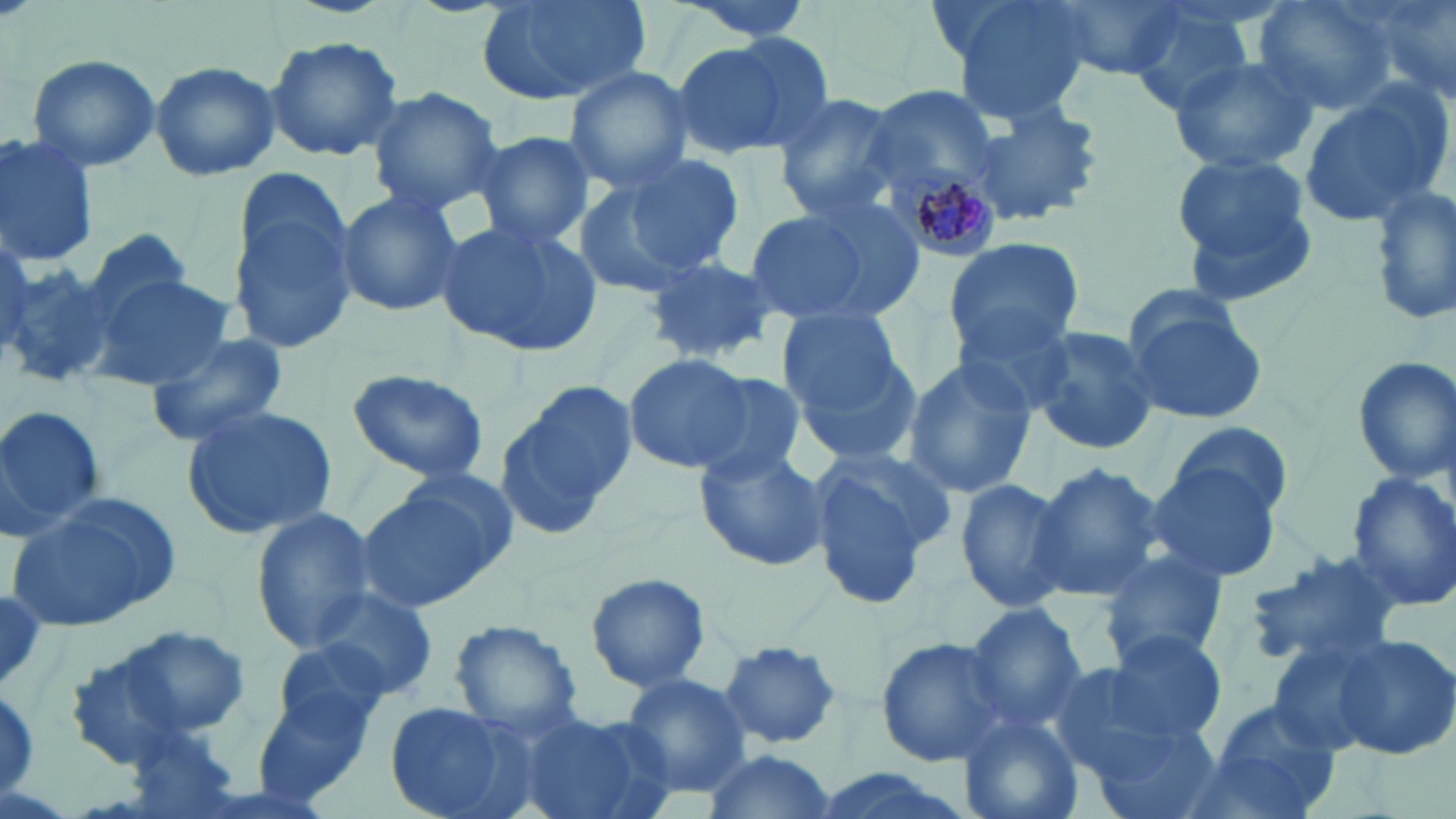

slide_level_diagnosis: Plasmodium malariae
modality: optical microscopy
uninfected_red_blood_cell_locations: 'approximate bounding boxes as named x1/y1/x2/y2 corners in pixels: (x1=475, y1=0, x2=648, y2=106), (x1=668, y1=0, x2=823, y2=42), (x1=941, y1=0, x2=1095, y2=125), (x1=1049, y1=0, x2=1187, y2=80), (x1=1125, y1=0, x2=1260, y2=111), (x1=1253, y1=0, x2=1397, y2=116), (x1=1358, y1=0, x2=1455, y2=110), (x1=672, y1=34, x2=827, y2=162), (x1=265, y1=35, x2=404, y2=162), (x1=26, y1=53, x2=161, y2=174), (x1=1167, y1=53, x2=1319, y2=174), (x1=150, y1=58, x2=281, y2=181), (x1=562, y1=65, x2=696, y2=190), (x1=363, y1=83, x2=506, y2=217), (x1=856, y1=83, x2=999, y2=189), (x1=1299, y1=83, x2=1452, y2=227), (x1=768, y1=90, x2=904, y2=221), (x1=963, y1=96, x2=1106, y2=228), (x1=472, y1=130, x2=597, y2=248), (x1=0, y1=133, x2=100, y2=268), (x1=613, y1=152, x2=745, y2=278), (x1=1170, y1=152, x2=1320, y2=299), (x1=226, y1=168, x2=361, y2=349), (x1=568, y1=175, x2=694, y2=298), (x1=1369, y1=186, x2=1456, y2=327), (x1=334, y1=188, x2=463, y2=318), (x1=739, y1=200, x2=909, y2=328), (x1=437, y1=219, x2=604, y2=358), (x1=73, y1=227, x2=197, y2=342), (x1=943, y1=237, x2=1085, y2=359), (x1=644, y1=256, x2=784, y2=366), (x1=0, y1=260, x2=120, y2=392), (x1=86, y1=269, x2=231, y2=394), (x1=1121, y1=300, x2=1264, y2=426), (x1=950, y1=301, x2=1080, y2=417), (x1=776, y1=306, x2=921, y2=459), (x1=1025, y1=322, x2=1160, y2=457), (x1=147, y1=332, x2=290, y2=447), (x1=623, y1=353, x2=755, y2=473), (x1=1350, y1=355, x2=1455, y2=486), (x1=902, y1=356, x2=1035, y2=500), (x1=344, y1=367, x2=490, y2=486), (x1=683, y1=370, x2=810, y2=481), (x1=496, y1=378, x2=637, y2=541), (x1=0, y1=403, x2=105, y2=541), (x1=180, y1=404, x2=337, y2=539), (x1=1170, y1=420, x2=1291, y2=521), (x1=694, y1=444, x2=830, y2=570), (x1=806, y1=448, x2=952, y2=611), (x1=1147, y1=458, x2=1283, y2=585), (x1=1028, y1=462, x2=1167, y2=603), (x1=1345, y1=471, x2=1456, y2=614), (x1=354, y1=475, x2=513, y2=615), (x1=951, y1=477, x2=1073, y2=613), (x1=6, y1=492, x2=183, y2=635), (x1=248, y1=509, x2=379, y2=652), (x1=1096, y1=547, x2=1232, y2=667), (x1=1239, y1=549, x2=1408, y2=672), (x1=584, y1=570, x2=712, y2=693), (x1=310, y1=586, x2=440, y2=703), (x1=961, y1=601, x2=1089, y2=729), (x1=448, y1=619, x2=583, y2=736), (x1=114, y1=623, x2=251, y2=738), (x1=1102, y1=628, x2=1229, y2=744), (x1=875, y1=635, x2=1012, y2=764), (x1=1332, y1=635, x2=1456, y2=759), (x1=272, y1=636, x2=398, y2=740), (x1=1264, y1=638, x2=1391, y2=756), (x1=718, y1=642, x2=843, y2=749), (x1=60, y1=648, x2=201, y2=770), (x1=1044, y1=663, x2=1183, y2=781), (x1=619, y1=671, x2=752, y2=799), (x1=255, y1=677, x2=383, y2=804), (x1=0, y1=680, x2=41, y2=802), (x1=1197, y1=700, x2=1345, y2=818), (x1=385, y1=702, x2=536, y2=819), (x1=512, y1=711, x2=678, y2=819), (x1=955, y1=711, x2=1084, y2=819), (x1=1089, y1=721, x2=1224, y2=819), (x1=117, y1=723, x2=245, y2=819), (x1=697, y1=747, x2=837, y2=818), (x1=803, y1=767, x2=978, y2=819)'
image_size: 1456×819 pixels
magnification: 1000x
stain: May-Grünwald-Giemsa
plasmodium_malariae_infected_red_blood_cell_locations: 'approximate bounding boxes as named x1/y1/x2/y2 corners in pixels: (x1=884, y1=162, x2=1001, y2=261)'
preparation: thin blood film
field_of_view: one of a larger specimen